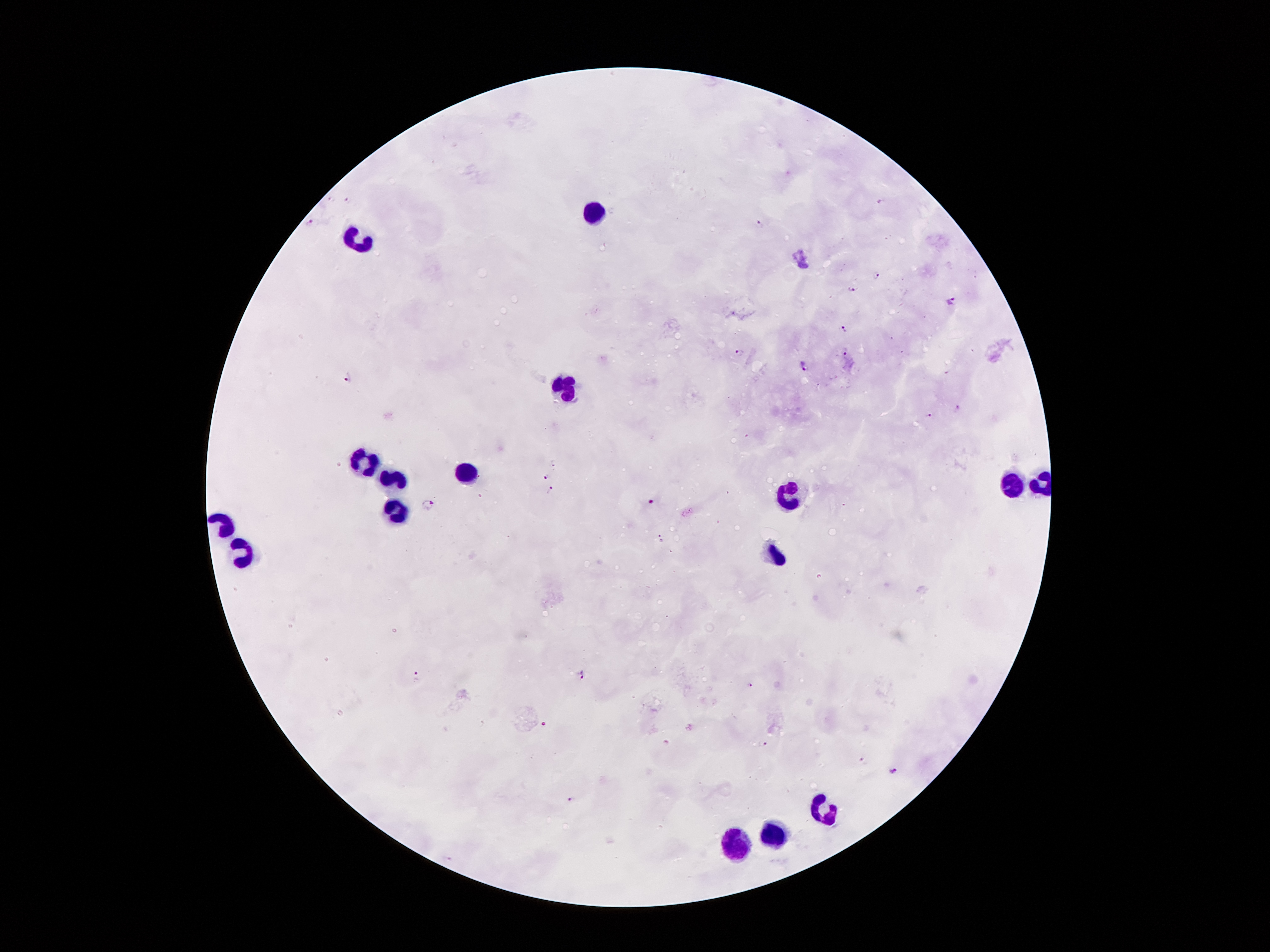
coordinate format = approximate centers as [x, y] in pixels
leukocyte locations = [596, 214], [362, 236], [562, 387], [368, 464], [463, 473], [393, 481], [1011, 487], [788, 494], [396, 510], [245, 552], [778, 560], [820, 807], [778, 833], [737, 846]
malaria parasite locations = [346, 200], [310, 223], [761, 225], [874, 276], [853, 288], [952, 302], [844, 328], [845, 352], [738, 354], [804, 365], [350, 377], [956, 408], [928, 417], [544, 477], [551, 488], [650, 502], [429, 504], [581, 675], [418, 677], [750, 685], [542, 725], [763, 746], [864, 761], [895, 771], [571, 800]
capture = smartphone through the microscope eyepiece
field of view = one from this slide
stain = Giemsa
patient malaria status = positive for Plasmodium falciparum
image size = 1270×952 pixels
magnification = 100x
preparation = thick peripheral-blood smear